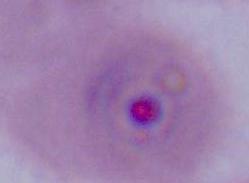

identification = Plasmodium
modality = photomicrograph
magnification = 400x or 1000x